Name the parasite shown.
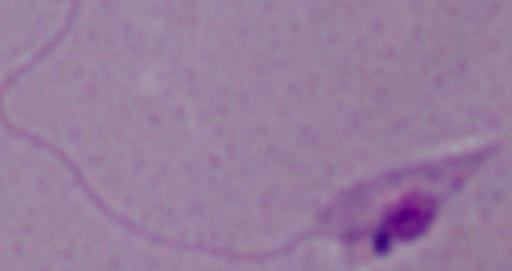

This is Leishmania.

Summary:
  - Modality: micrograph
  - Magnification: 1000x